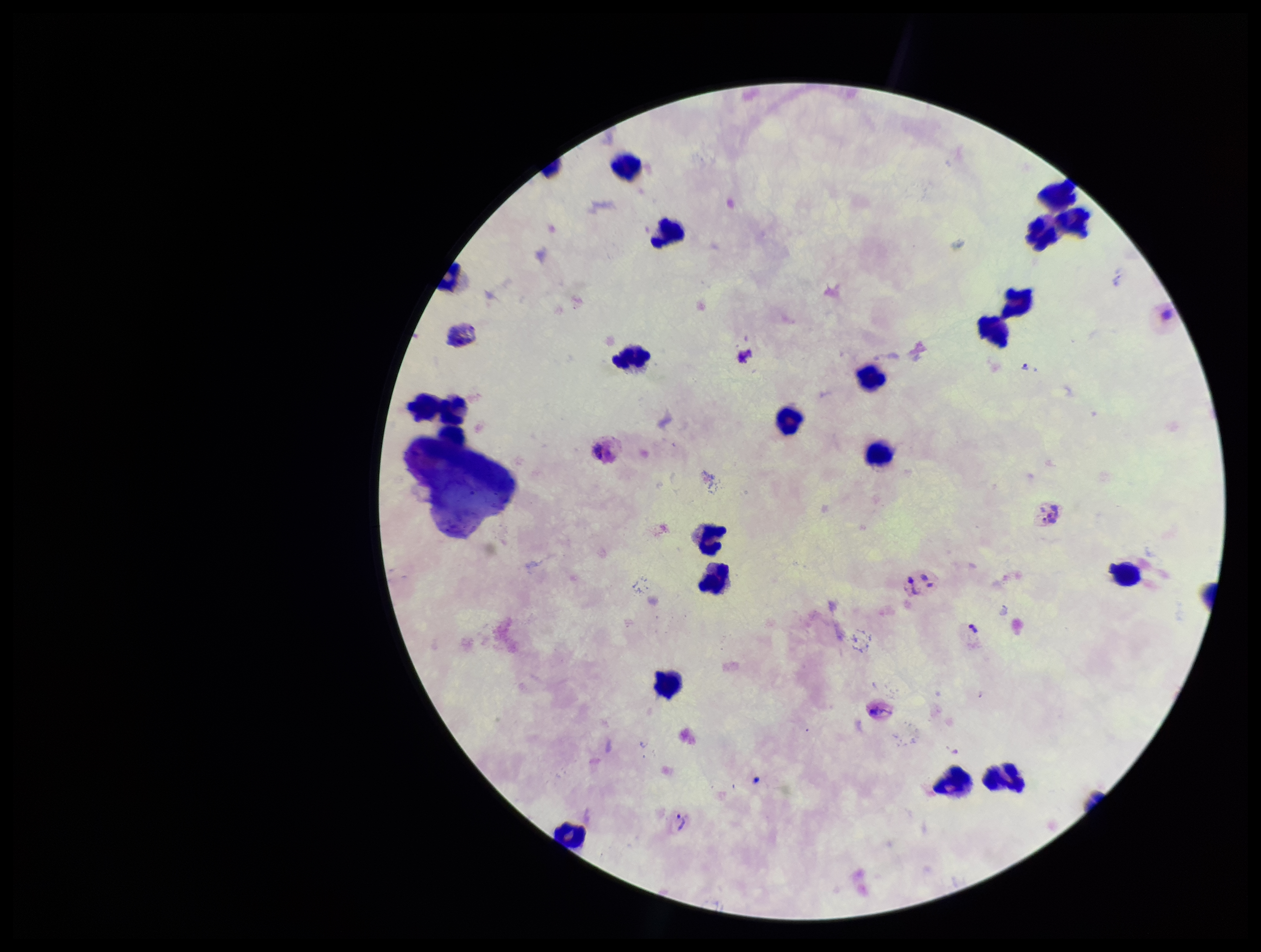
Summary:
  - Patient malaria status: positive
  - Capture: smartphone photograph through the microscope eyepiece
  - Plasmodium parasites: none identified
  - Leukocyte count: 20
  - Image size: 1261×952 pixels
  - Stain: Giemsa
  - Preparation: thick blood smear
  - Species reported for this patient: Plasmodium vivax
  - Field of view: one from this slide
  - Parasite count: 0